Locate every blood parasite and identify its species.
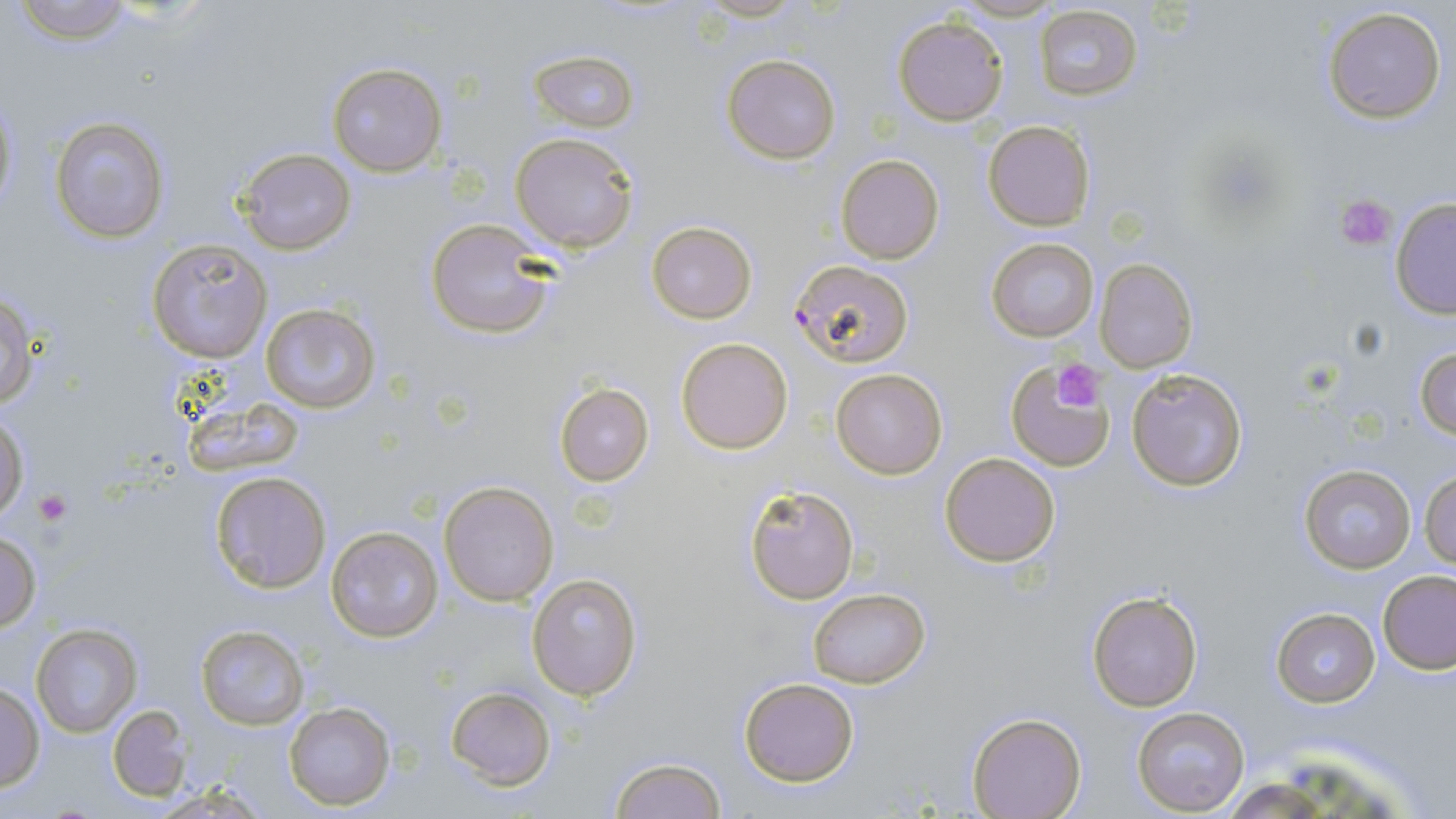

Approximate bounding boxes as [x1, y1, x2, y2] in pixels.
Plasmodium falciparum-infected red blood cells: [788, 259, 913, 368].
No Plasmodium ovale, Plasmodium malariae, Plasmodium vivax, Babesia divergens, or Trypanosoma brucei observed.

{
  "slide_level_diagnosis": "Plasmodium falciparum",
  "image_size": "1456×819 pixels",
  "platelet_locations": "approximate bounding boxes as [x1, y1, x2, y2] in pixels: [1337, 194, 1397, 251], [1052, 359, 1106, 412], [34, 488, 73, 526]",
  "magnification": "1000x",
  "modality": "optical microscopy",
  "preparation": "thin blood smear",
  "uninfected_red_blood_cell_locations": "approximate bounding boxes as [x1, y1, x2, y2] in pixels: [9, 0, 133, 45], [948, 1, 1060, 23], [1034, 5, 1146, 102], [1322, 6, 1446, 124], [893, 16, 1006, 126], [528, 49, 638, 131], [721, 54, 841, 164], [327, 62, 447, 175], [1, 96, 19, 217], [51, 116, 169, 243], [983, 120, 1096, 231], [510, 132, 639, 252], [236, 147, 356, 257], [836, 154, 944, 265], [1390, 199, 1455, 319], [424, 219, 555, 341], [646, 220, 757, 323], [986, 237, 1099, 342], [146, 239, 270, 361], [1094, 258, 1198, 373], [0, 292, 36, 412], [260, 304, 380, 414], [676, 337, 793, 454], [1414, 345, 1456, 441], [1004, 360, 1117, 472], [829, 367, 948, 479], [1126, 367, 1249, 493], [553, 383, 655, 487], [0, 413, 28, 521], [939, 452, 1061, 567], [1298, 465, 1418, 574], [208, 470, 333, 594], [1420, 470, 1456, 569], [438, 481, 558, 606], [744, 485, 858, 604], [326, 527, 446, 643], [1, 532, 41, 629], [1378, 570, 1456, 673], [526, 571, 643, 700], [807, 586, 930, 690], [1087, 589, 1204, 711], [1270, 608, 1381, 707], [29, 623, 142, 738], [194, 624, 310, 731], [737, 677, 860, 787], [0, 684, 46, 792], [444, 686, 557, 789], [282, 700, 396, 810], [109, 705, 192, 802], [1132, 707, 1251, 815], [967, 711, 1086, 818], [607, 756, 726, 818]",
  "stain": "May-Grünwald-Giemsa",
  "field_of_view": "one of a larger specimen"
}